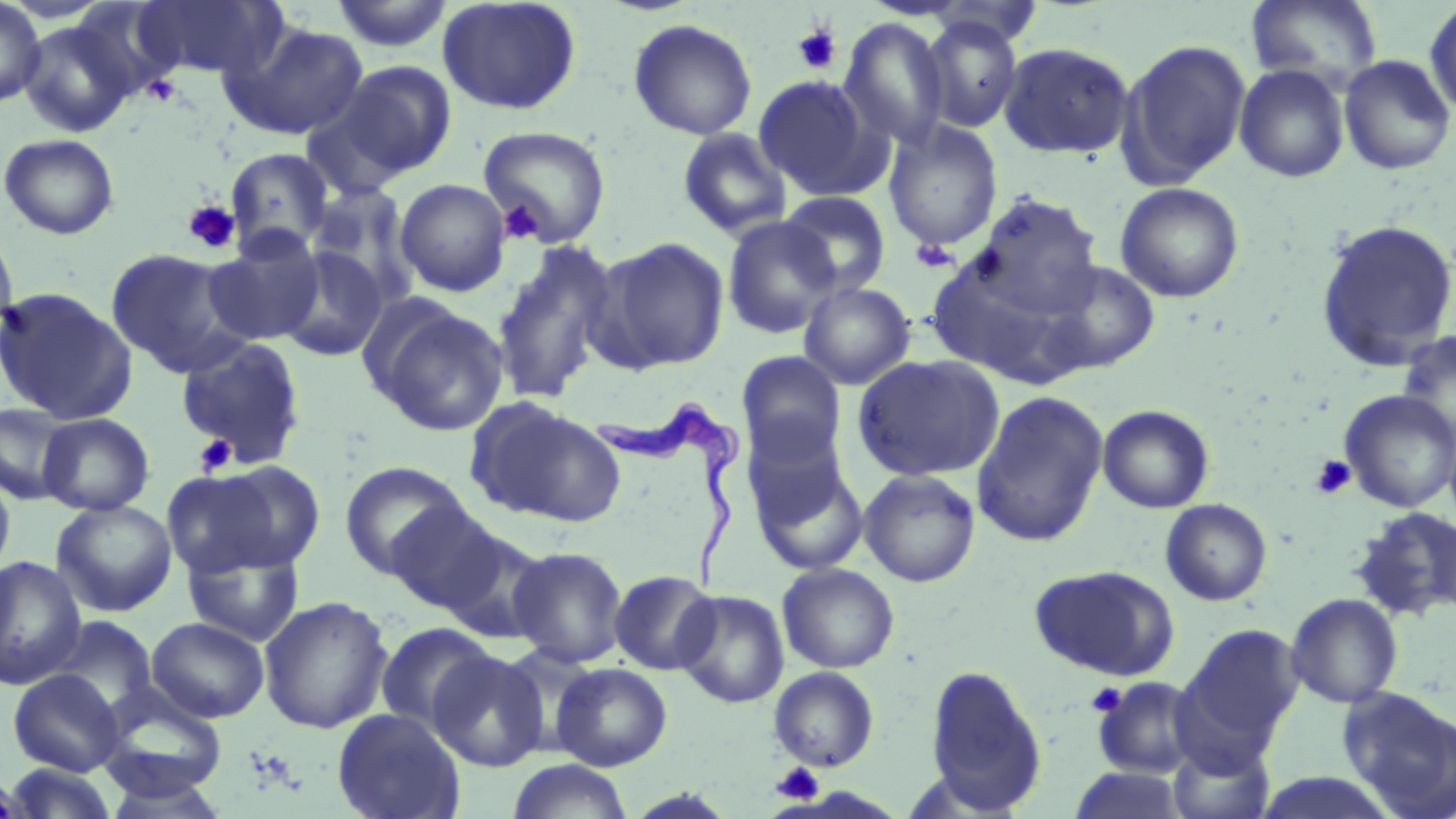
slide-level diagnosis = Trypanosoma brucei
modality = light microscopy
preparation = thin blood smear
uninfected red blood cell locations = approximate bounding boxes as [x1, y1, x2, y2] in pixels: [0, 0, 46, 108], [131, 0, 285, 81], [438, 0, 582, 115], [1246, 0, 1383, 89], [328, 1, 456, 52], [1423, 1, 1456, 119], [921, 16, 1023, 133], [17, 17, 139, 138], [628, 18, 757, 140], [840, 18, 949, 150], [219, 21, 368, 141], [1117, 38, 1253, 188], [998, 42, 1135, 159], [1338, 54, 1455, 176], [330, 60, 457, 182], [1234, 64, 1350, 183], [753, 75, 883, 200], [883, 120, 1003, 252], [477, 125, 612, 248], [677, 128, 793, 240], [1, 133, 120, 239], [225, 147, 335, 255], [395, 179, 511, 297], [1115, 182, 1244, 302], [307, 184, 420, 306], [778, 191, 891, 297], [971, 193, 1103, 315], [723, 216, 840, 338], [1315, 218, 1456, 371], [0, 224, 19, 347], [202, 232, 325, 346], [594, 236, 731, 373], [490, 239, 620, 405], [276, 246, 389, 362], [106, 248, 247, 377], [924, 255, 1084, 386], [1040, 259, 1161, 374], [799, 281, 916, 390], [0, 286, 137, 424], [376, 305, 508, 437], [1396, 328, 1455, 453], [175, 335, 308, 469], [736, 351, 848, 466], [852, 354, 1005, 481], [1339, 389, 1456, 512], [972, 391, 1108, 547], [0, 402, 76, 506], [471, 402, 626, 527], [1097, 404, 1215, 513], [37, 413, 155, 516], [747, 447, 868, 575], [198, 459, 327, 573], [339, 461, 473, 579], [0, 470, 16, 582], [859, 470, 981, 587], [1160, 498, 1273, 605], [51, 500, 178, 617], [384, 501, 509, 614], [1350, 506, 1456, 622], [438, 528, 551, 644], [182, 542, 306, 647], [508, 546, 628, 668], [0, 556, 87, 690], [777, 563, 900, 673], [1029, 564, 1179, 681], [609, 570, 719, 675], [675, 590, 789, 708], [1285, 593, 1403, 708], [258, 596, 394, 733], [45, 617, 159, 716], [147, 617, 270, 722], [375, 622, 499, 737], [1180, 623, 1304, 749], [428, 650, 549, 772], [551, 662, 673, 771], [923, 666, 1047, 813], [769, 667, 880, 771], [8, 669, 125, 776], [1091, 676, 1203, 778], [96, 684, 227, 801], [1338, 685, 1456, 818], [331, 708, 466, 819], [1166, 738, 1275, 819], [505, 759, 635, 819], [4, 763, 121, 819], [1068, 766, 1190, 818], [1, 768, 32, 819], [1250, 770, 1401, 818]
stain = May-Grünwald-Giemsa
Trypanosoma brucei locations = approximate bounding boxes as [x1, y1, x2, y2] in pixels: [599, 400, 736, 599]
image size = 1456×819 pixels
field of view = one of a larger specimen
magnification = 1000x
platelet locations = approximate bounding boxes as [x1, y1, x2, y2] in pixels: [792, 23, 842, 74], [143, 74, 182, 106], [182, 200, 240, 254], [498, 200, 542, 243], [911, 239, 957, 272], [194, 434, 237, 476], [1310, 455, 1356, 500], [1087, 683, 1127, 717], [771, 762, 825, 805]